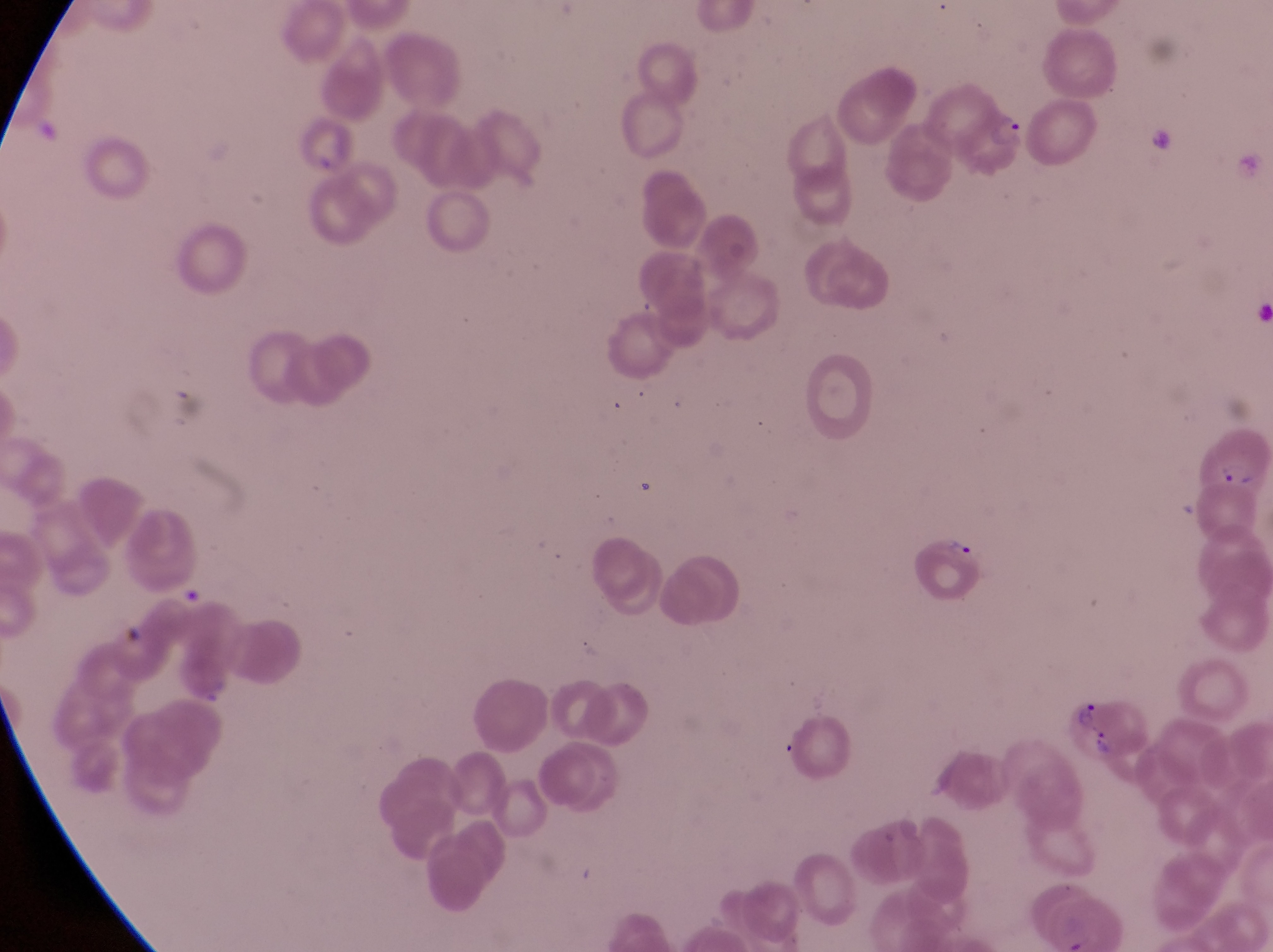
Approximate bounding boxes as left top right bottom in pixels.
Summary:
  - Artifact (platelet-like body, stain precipitate, or debris) locations: 175 579 205 611
  - Parasitised red blood cell locations: 1196 419 1271 494; 1066 689 1154 771
  - Trophozoite locations: 988 112 1030 151; 943 529 973 569
  - Preparation: thin blood film
  - Country: Uganda
  - Magnification: 1000x
  - Image size: 1273×952 pixels
  - Capture: smartphone photograph through the eyepiece of an Olympus CX-23 microscope
  - Field of view: single